Locate platelets.
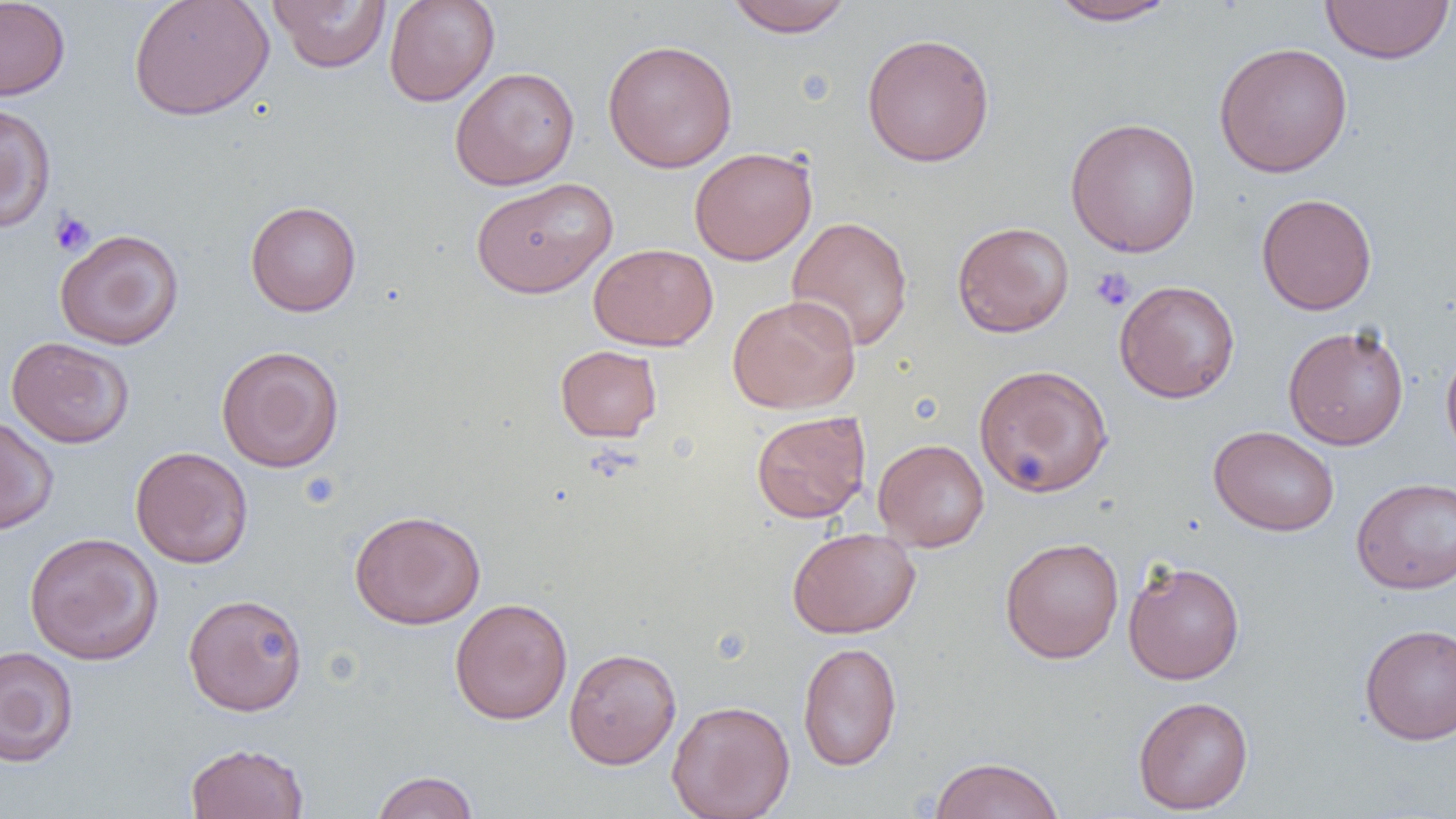
Approximate bounding boxes as named x1/y1/x2/y2 corners in pixels.
Platelets: (x1=49, y1=209, x2=95, y2=256), (x1=1089, y1=266, x2=1136, y2=312).

slide_level_diagnosis: negative for blood parasites
uninfected_red_blood_cell_locations: 'approximate bounding boxes as named x1/y1/x2/y2 corners in pixels: (x1=0, y1=0, x2=71, y2=101), (x1=128, y1=0, x2=275, y2=121), (x1=384, y1=0, x2=499, y2=107), (x1=1046, y1=0, x2=1180, y2=26), (x1=1320, y1=0, x2=1455, y2=65), (x1=268, y1=1, x2=390, y2=72), (x1=724, y1=1, x2=854, y2=37), (x1=861, y1=31, x2=996, y2=167), (x1=602, y1=39, x2=738, y2=173), (x1=1213, y1=42, x2=1353, y2=177), (x1=449, y1=66, x2=580, y2=190), (x1=0, y1=104, x2=56, y2=233), (x1=1064, y1=117, x2=1201, y2=258), (x1=689, y1=146, x2=818, y2=265), (x1=470, y1=176, x2=617, y2=299), (x1=1257, y1=193, x2=1377, y2=315), (x1=245, y1=200, x2=362, y2=316), (x1=786, y1=215, x2=914, y2=353), (x1=951, y1=221, x2=1075, y2=338), (x1=54, y1=228, x2=184, y2=350), (x1=588, y1=243, x2=718, y2=351), (x1=1114, y1=280, x2=1240, y2=403), (x1=726, y1=294, x2=861, y2=414), (x1=1282, y1=324, x2=1409, y2=450), (x1=6, y1=336, x2=134, y2=448), (x1=216, y1=345, x2=345, y2=473), (x1=555, y1=345, x2=663, y2=442), (x1=1441, y1=346, x2=1456, y2=466), (x1=973, y1=363, x2=1114, y2=498), (x1=751, y1=410, x2=871, y2=523), (x1=0, y1=415, x2=59, y2=535), (x1=1208, y1=425, x2=1340, y2=536), (x1=873, y1=438, x2=990, y2=552), (x1=130, y1=446, x2=253, y2=569), (x1=1351, y1=477, x2=1456, y2=594), (x1=348, y1=509, x2=486, y2=630), (x1=787, y1=526, x2=920, y2=639), (x1=24, y1=532, x2=163, y2=665), (x1=999, y1=536, x2=1124, y2=664), (x1=1123, y1=559, x2=1245, y2=685), (x1=183, y1=593, x2=308, y2=716), (x1=449, y1=597, x2=573, y2=725), (x1=1359, y1=623, x2=1456, y2=744), (x1=797, y1=641, x2=902, y2=771), (x1=0, y1=646, x2=79, y2=767), (x1=563, y1=647, x2=682, y2=769), (x1=1133, y1=695, x2=1254, y2=814), (x1=667, y1=699, x2=795, y2=819), (x1=184, y1=742, x2=310, y2=819), (x1=928, y1=755, x2=1066, y2=819), (x1=370, y1=770, x2=480, y2=819)'
magnification: 1000x
image_size: 1456×819 pixels
field_of_view: one of a larger specimen
modality: optical microscopy
preparation: thin blood film